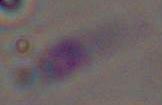
Toxoplasma gondii is shown. Captured at 1000x magnification. Micrograph.